Comment on the morphology of the erythrocytes.
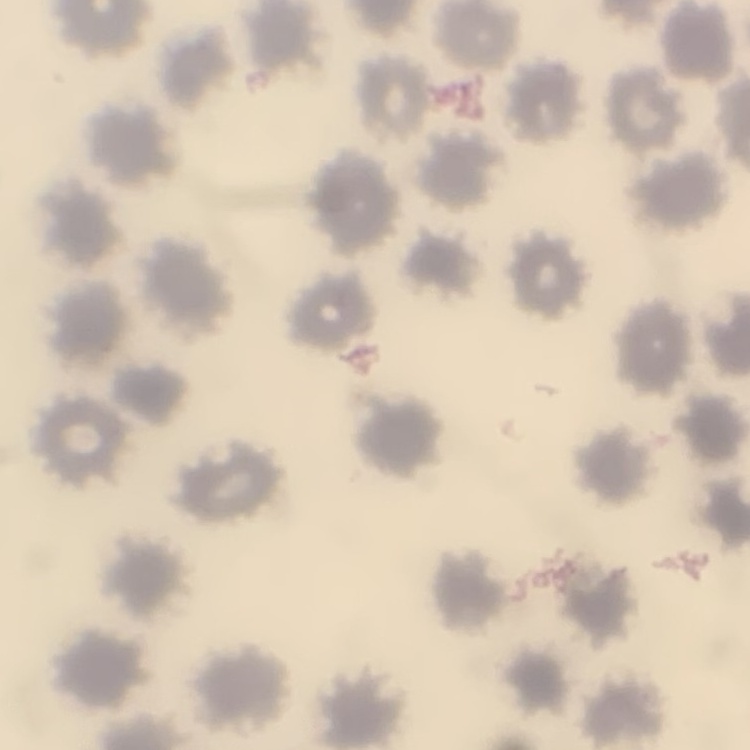
No rouleaux formation.

image type = one tile cut from a larger photomicrograph
stain = Field's or Giemsa
preparation = thin blood film